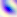

Toxoplasma gondii is shown. Micrograph. Captured at 400x magnification.